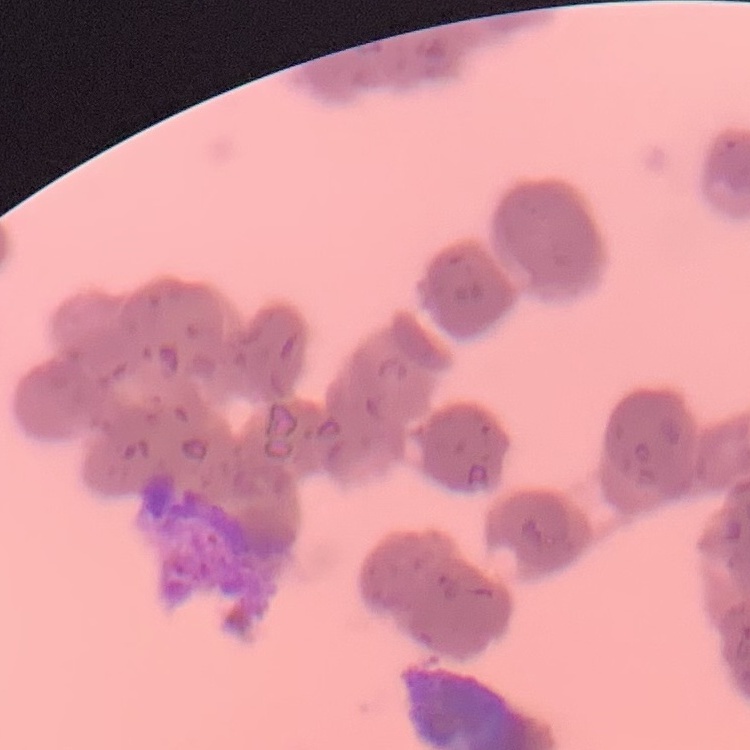

erythrocyte morphology = rouleaux formation
image type = one tile cut from a larger photomicrograph
stain = Field's or Giemsa
preparation = thin blood smear